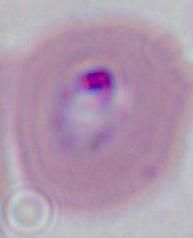
Summary:
  - Magnification: 400x or 1000x
  - Modality: photomicrograph
  - Identification: Plasmodium